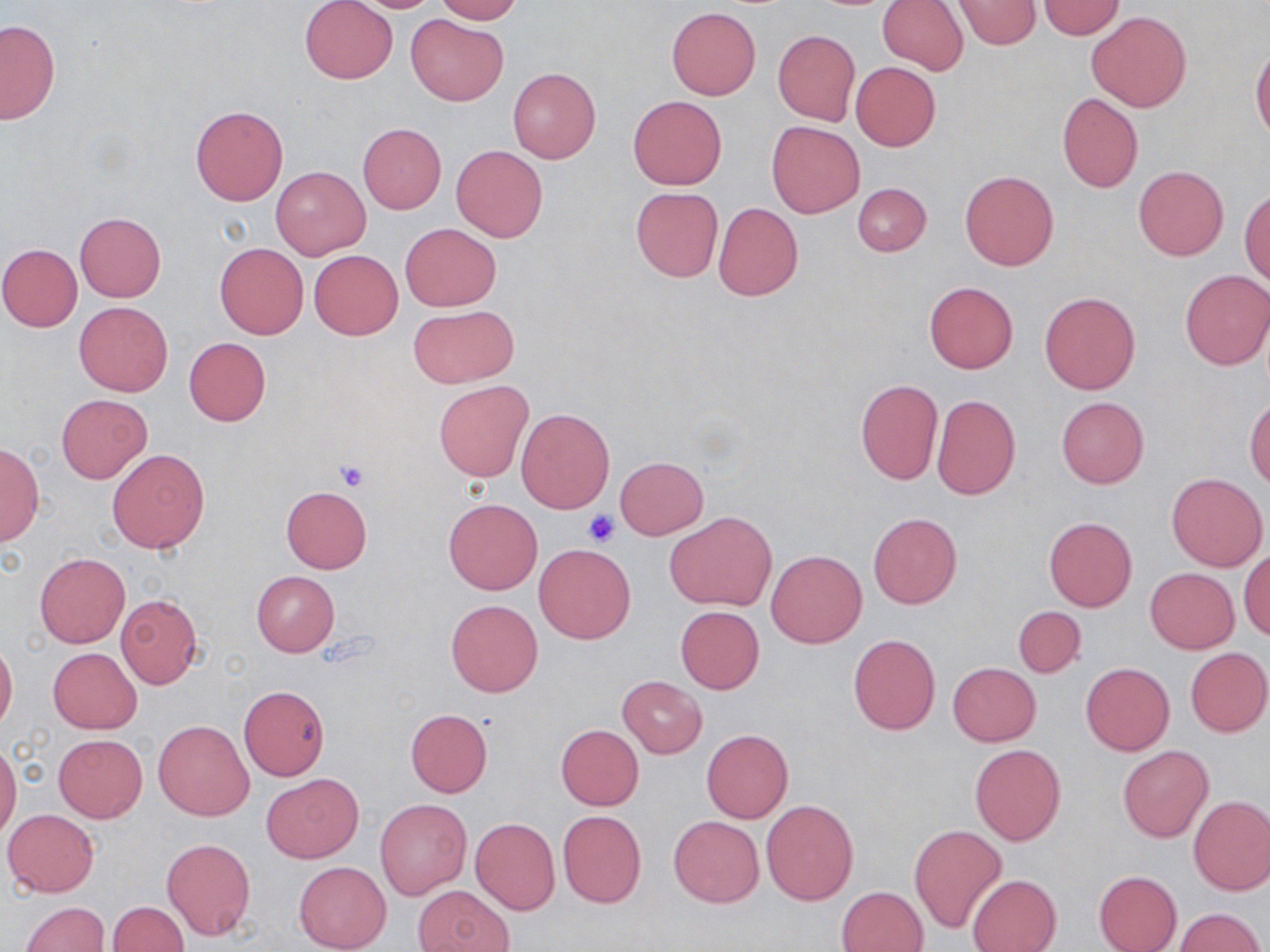

Approximate bounding boxes as (x1, y1, x2, y2) in pixels. Uninfected red blood cell locations: (299, 0, 398, 85), (343, 0, 446, 12), (434, 0, 522, 23), (878, 0, 968, 75), (952, 0, 1042, 50), (1038, 1, 1126, 39), (665, 6, 761, 100), (1086, 12, 1193, 112), (405, 14, 508, 105), (0, 20, 60, 125), (772, 29, 860, 126), (1251, 44, 1270, 142), (850, 61, 941, 151), (507, 68, 600, 163), (1056, 93, 1143, 193), (628, 95, 727, 190), (190, 105, 287, 205), (766, 121, 865, 218), (357, 123, 446, 214), (451, 145, 548, 242), (270, 166, 371, 261), (1133, 166, 1228, 260), (960, 170, 1059, 271), (853, 182, 931, 256), (1240, 187, 1269, 284), (630, 188, 723, 282), (713, 202, 803, 301), (75, 213, 166, 302), (399, 224, 502, 310), (214, 242, 309, 339), (0, 243, 83, 331), (308, 249, 403, 340), (1180, 269, 1270, 370), (924, 281, 1018, 373), (1039, 291, 1140, 394), (74, 301, 172, 395), (409, 305, 520, 388), (184, 337, 270, 426), (433, 380, 533, 481), (854, 380, 943, 485), (57, 394, 151, 483), (932, 395, 1020, 500), (1055, 397, 1149, 489), (1246, 397, 1270, 489), (516, 407, 615, 513), (0, 443, 43, 548), (106, 448, 210, 554), (615, 456, 707, 539), (1166, 473, 1267, 572), (280, 485, 372, 573), (443, 497, 542, 595), (665, 511, 776, 610), (868, 512, 961, 609), (1044, 516, 1136, 611), (535, 544, 634, 644), (766, 550, 866, 648), (1240, 550, 1270, 640), (35, 553, 129, 648), (1145, 567, 1239, 654), (252, 571, 340, 656), (116, 594, 203, 689), (446, 599, 543, 697), (675, 605, 763, 694), (1012, 605, 1086, 678), (848, 634, 940, 735), (0, 639, 18, 732), (1184, 647, 1270, 738), (48, 648, 141, 734), (948, 662, 1040, 746), (1081, 663, 1174, 756), (617, 676, 706, 758), (238, 684, 330, 781), (405, 709, 492, 796), (154, 719, 253, 820), (556, 725, 644, 809), (701, 729, 793, 822), (53, 734, 147, 822), (0, 740, 21, 840), (969, 744, 1065, 845), (1118, 745, 1214, 843), (261, 773, 364, 863), (1188, 795, 1270, 895), (374, 799, 471, 900), (761, 800, 858, 905), (3, 808, 99, 896), (557, 810, 647, 908), (669, 816, 764, 907), (469, 817, 560, 915), (909, 824, 1007, 933), (162, 838, 255, 940), (295, 861, 392, 952), (1093, 870, 1181, 952), (967, 874, 1061, 952), (837, 886, 928, 952), (413, 887, 511, 951), (106, 901, 189, 952), (20, 902, 109, 952), (1173, 907, 1264, 951). Platelet locations: (336, 461, 369, 492), (582, 511, 620, 547). Slide-level diagnosis: no evidence of blood parasites. Image is 1270×952 pixels. Thin blood film. 1000x magnification. Single field of view. May-Grünwald-Giemsa stain. Optical microscopy.